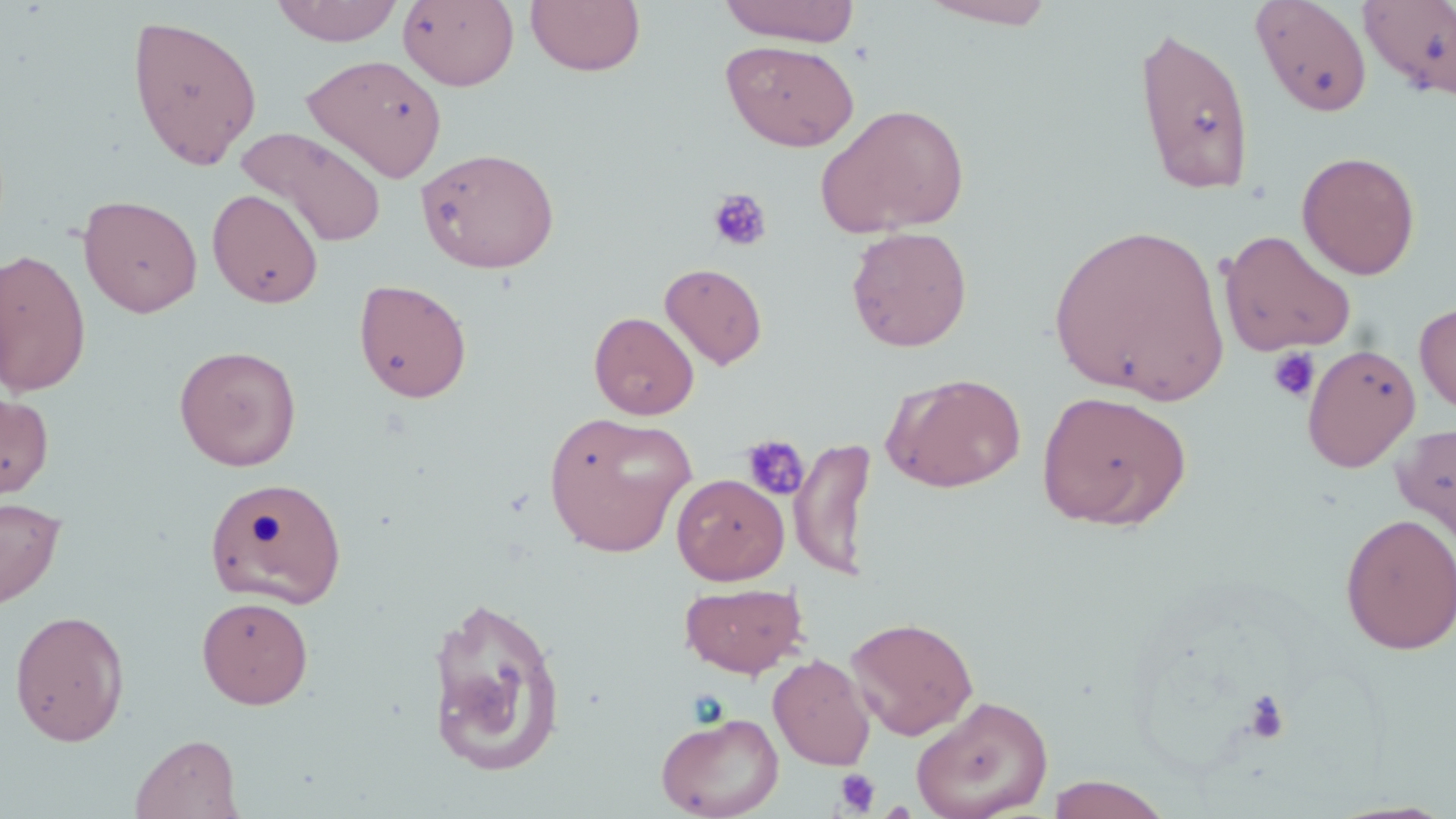

{
  "slide_level_diagnosis": "negative for blood parasites",
  "image_size": "1456×819 pixels",
  "magnification": "1000x",
  "field_of_view": "single",
  "modality": "light microscopy",
  "stain": "May-Grünwald-Giemsa",
  "uninfected_red_blood_cell_locations": "approximate bounding boxes as (x1, y1, x2, y2) in pixels: (273, 0, 404, 46), (398, 0, 519, 90), (525, 0, 646, 77), (917, 0, 1062, 29), (1250, 0, 1374, 118), (717, 1, 862, 46), (1358, 1, 1456, 99), (127, 13, 263, 171), (1133, 23, 1256, 195), (722, 40, 859, 151), (303, 54, 447, 181), (816, 103, 970, 238), (237, 127, 387, 249), (415, 147, 560, 274), (1296, 151, 1421, 279), (207, 188, 323, 309), (78, 194, 203, 318), (1047, 221, 1231, 404), (846, 226, 972, 352), (1218, 229, 1357, 357), (0, 248, 92, 397), (660, 262, 768, 370), (353, 277, 472, 403), (1415, 301, 1456, 415), (589, 312, 699, 420), (1302, 343, 1421, 472), (174, 344, 302, 471), (883, 372, 1027, 493), (0, 390, 55, 500), (1036, 391, 1192, 530), (543, 411, 696, 558), (1391, 421, 1456, 552), (791, 436, 876, 580), (671, 473, 789, 585), (204, 475, 347, 609), (0, 495, 66, 610), (1340, 512, 1456, 655), (679, 581, 807, 679), (423, 592, 567, 777), (197, 595, 314, 709), (9, 609, 130, 747), (845, 616, 979, 740), (768, 653, 876, 770), (911, 696, 1053, 819), (656, 711, 784, 819), (129, 733, 243, 818), (1045, 775, 1172, 819)",
  "preparation": "thin blood film",
  "platelet_locations": "approximate bounding boxes as (x1, y1, x2, y2) in pixels: (707, 188, 773, 252), (1266, 346, 1321, 403), (741, 435, 810, 502), (1243, 689, 1291, 745), (835, 768, 881, 816)"
}